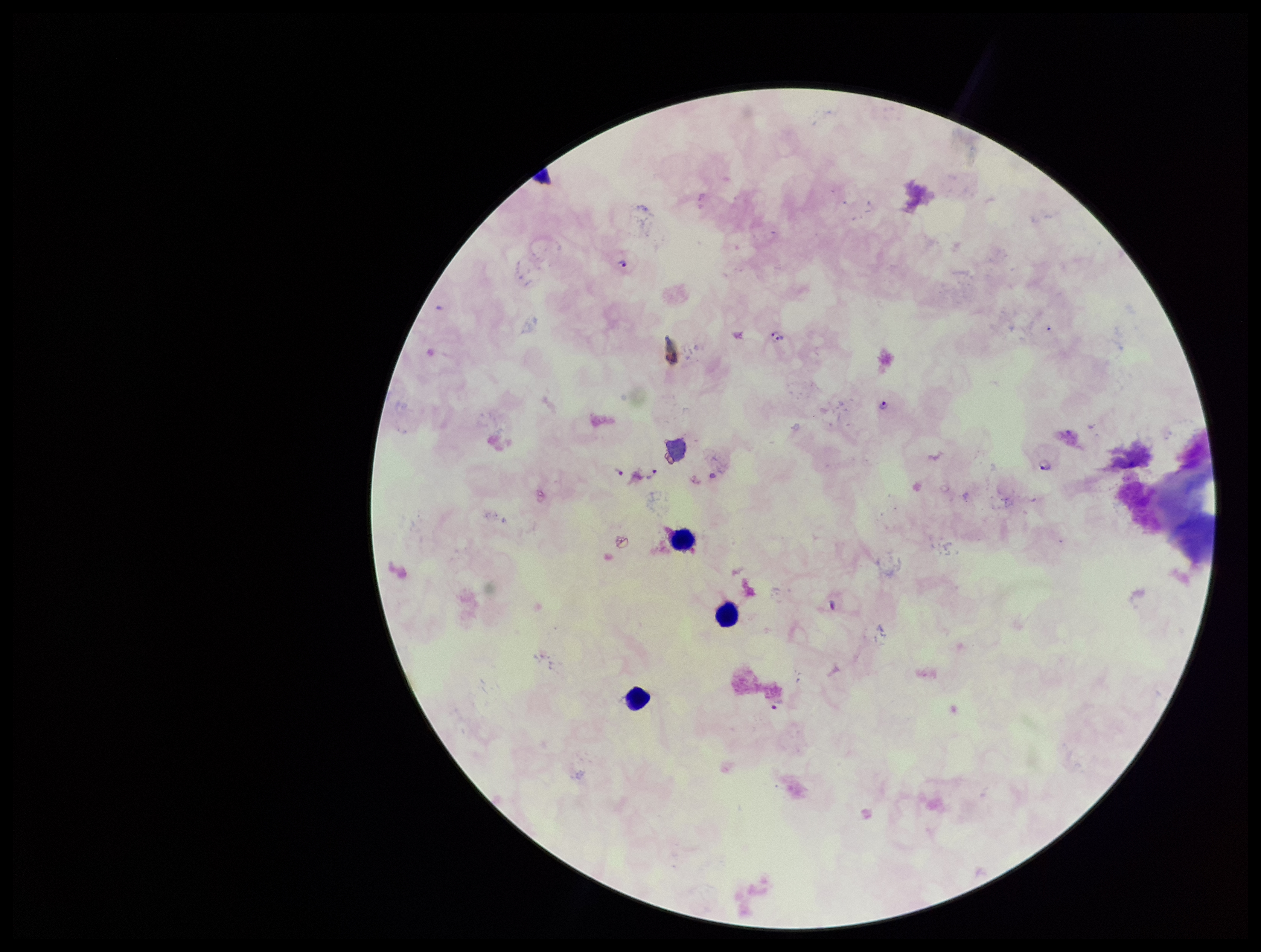

{
  "stain": "Giemsa",
  "capture": "smartphone photograph through the microscope eyepiece",
  "image_size": "1261×952 pixels",
  "leukocyte_count": 3,
  "patient_malaria_status": "positive",
  "plasmodium_parasites": "identified",
  "parasite_count": 7,
  "field_of_view": "single",
  "species_reported_for_this_patient": "Plasmodium falciparum",
  "preparation": "thick"
}